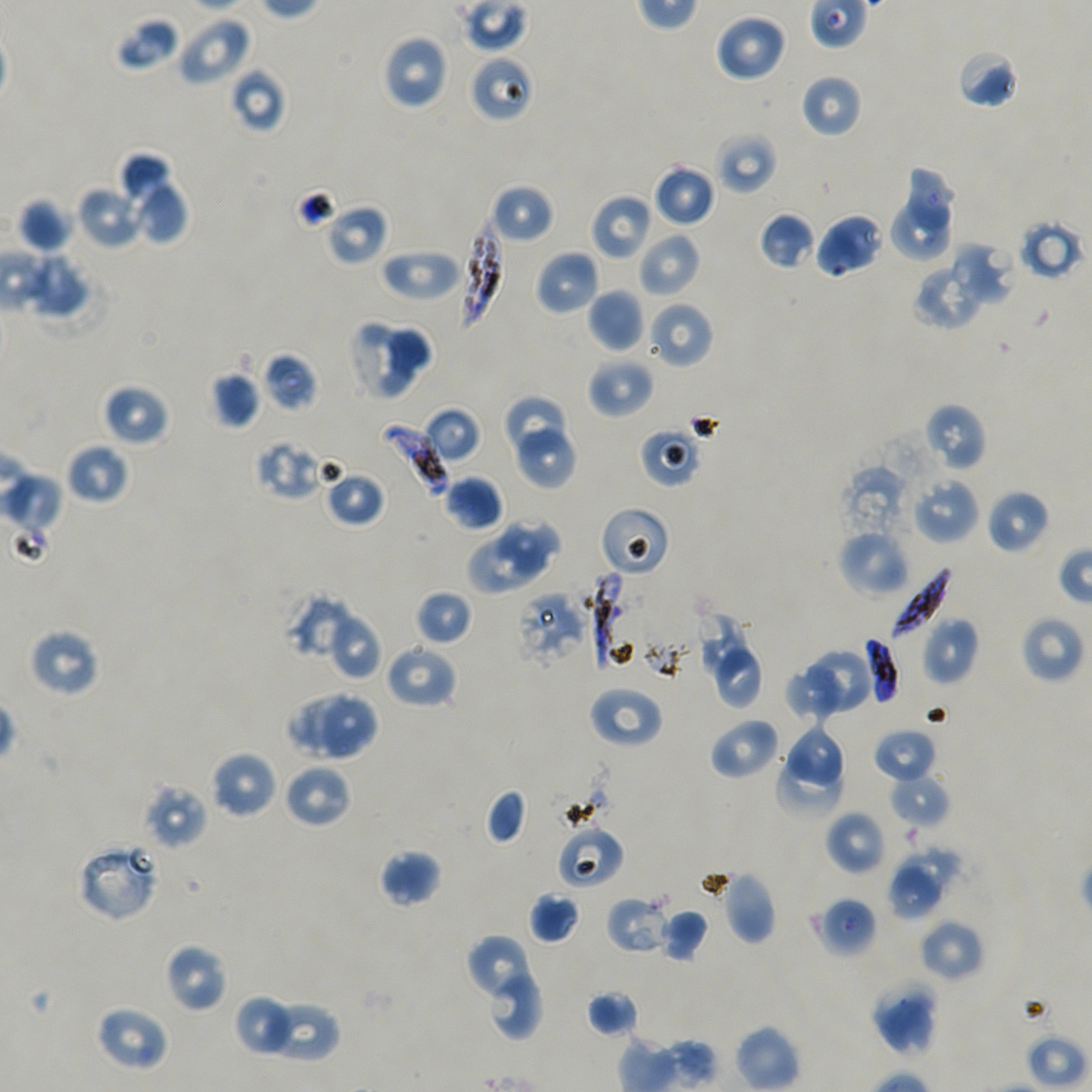

Approximate bounding rectangles given as corner coordinates in pixels from the top-left. Not every red blood cell is marked.
Summary:
  - Locations of infected red blood cells: (x1=459, y1=216, x2=504, y2=329), (x1=378, y1=422, x2=449, y2=498), (x1=886, y1=567, x2=952, y2=640), (x1=587, y1=569, x2=639, y2=670), (x1=864, y1=636, x2=900, y2=706)
  - Locations of uninfected red blood cells: (x1=714, y1=13, x2=788, y2=83), (x1=175, y1=15, x2=252, y2=86), (x1=115, y1=16, x2=181, y2=71), (x1=381, y1=34, x2=450, y2=110), (x1=956, y1=48, x2=1019, y2=109), (x1=230, y1=68, x2=287, y2=133), (x1=799, y1=73, x2=862, y2=138), (x1=714, y1=131, x2=778, y2=194), (x1=117, y1=152, x2=173, y2=207), (x1=653, y1=163, x2=716, y2=228), (x1=905, y1=164, x2=954, y2=231), (x1=133, y1=183, x2=189, y2=246), (x1=489, y1=183, x2=554, y2=244), (x1=75, y1=187, x2=143, y2=249), (x1=590, y1=193, x2=653, y2=261), (x1=17, y1=196, x2=73, y2=253), (x1=886, y1=198, x2=953, y2=264), (x1=324, y1=203, x2=389, y2=266), (x1=759, y1=212, x2=815, y2=270), (x1=814, y1=212, x2=885, y2=278), (x1=637, y1=231, x2=702, y2=297), (x1=949, y1=242, x2=1017, y2=308), (x1=380, y1=247, x2=460, y2=301), (x1=534, y1=250, x2=600, y2=316), (x1=16, y1=251, x2=91, y2=319), (x1=912, y1=262, x2=985, y2=330), (x1=587, y1=288, x2=644, y2=352), (x1=647, y1=302, x2=714, y2=368), (x1=386, y1=322, x2=435, y2=378), (x1=347, y1=323, x2=414, y2=401), (x1=587, y1=356, x2=655, y2=419), (x1=210, y1=371, x2=261, y2=429), (x1=101, y1=383, x2=170, y2=447), (x1=506, y1=395, x2=565, y2=454), (x1=923, y1=402, x2=987, y2=472), (x1=422, y1=405, x2=481, y2=463), (x1=638, y1=425, x2=703, y2=487), (x1=517, y1=429, x2=576, y2=489), (x1=65, y1=442, x2=130, y2=505), (x1=1, y1=462, x2=62, y2=562), (x1=839, y1=466, x2=907, y2=547), (x1=321, y1=467, x2=386, y2=528), (x1=442, y1=475, x2=505, y2=532), (x1=911, y1=476, x2=980, y2=544), (x1=986, y1=489, x2=1050, y2=554), (x1=496, y1=518, x2=562, y2=577), (x1=837, y1=529, x2=909, y2=597), (x1=467, y1=532, x2=542, y2=596), (x1=415, y1=589, x2=473, y2=647), (x1=285, y1=592, x2=356, y2=661), (x1=327, y1=610, x2=382, y2=680), (x1=1019, y1=615, x2=1084, y2=685), (x1=697, y1=616, x2=750, y2=682), (x1=922, y1=617, x2=979, y2=685), (x1=28, y1=627, x2=100, y2=697), (x1=384, y1=642, x2=458, y2=709), (x1=810, y1=647, x2=875, y2=712), (x1=714, y1=648, x2=761, y2=710), (x1=786, y1=666, x2=844, y2=727), (x1=587, y1=685, x2=663, y2=749), (x1=285, y1=689, x2=352, y2=754), (x1=318, y1=693, x2=377, y2=761), (x1=708, y1=716, x2=781, y2=781), (x1=786, y1=728, x2=849, y2=786), (x1=873, y1=728, x2=936, y2=784), (x1=778, y1=748, x2=840, y2=824), (x1=209, y1=750, x2=278, y2=820), (x1=283, y1=764, x2=352, y2=829), (x1=887, y1=774, x2=950, y2=829), (x1=142, y1=782, x2=208, y2=851), (x1=485, y1=789, x2=527, y2=844), (x1=824, y1=809, x2=886, y2=876), (x1=556, y1=826, x2=624, y2=890), (x1=899, y1=845, x2=960, y2=895), (x1=379, y1=850, x2=442, y2=907), (x1=888, y1=865, x2=942, y2=920), (x1=718, y1=870, x2=777, y2=946), (x1=529, y1=892, x2=581, y2=945), (x1=605, y1=896, x2=669, y2=956), (x1=657, y1=908, x2=709, y2=962), (x1=918, y1=920, x2=984, y2=982), (x1=465, y1=935, x2=530, y2=998), (x1=164, y1=943, x2=228, y2=1013), (x1=488, y1=975, x2=545, y2=1040), (x1=871, y1=981, x2=939, y2=1055), (x1=586, y1=989, x2=639, y2=1038), (x1=233, y1=994, x2=289, y2=1052), (x1=96, y1=1005, x2=169, y2=1071), (x1=264, y1=1005, x2=340, y2=1063)
  - Locations of red blood cells of indeterminate infection status: (x1=469, y1=54, x2=534, y2=123), (x1=1016, y1=218, x2=1086, y2=281), (x1=263, y1=351, x2=318, y2=412), (x1=255, y1=439, x2=327, y2=500), (x1=599, y1=506, x2=670, y2=577), (x1=515, y1=591, x2=589, y2=668), (x1=77, y1=840, x2=162, y2=922), (x1=817, y1=896, x2=877, y2=958)
  - Image size: 1092×1092 pixels
  - Donor blood group: A+/O+
  - Field of view: single
  - Culture: P. falciparum strain NF54, static, in vitro
  - Objective: 100x, oil immersion, numerical aperture 1.45
  - Stain: Giemsa
  - Preparation: thin blood film